Assess this cell for malaria.
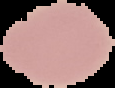
Uninfected.

image size = 115×88 pixels
preparation = thin blood film
image type = segmented cell region with the area outside set to black